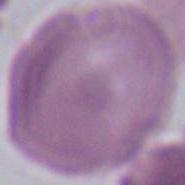
{
  "modality": "photomicrograph",
  "magnification": "1000x",
  "identification": "erythrocyte"
}